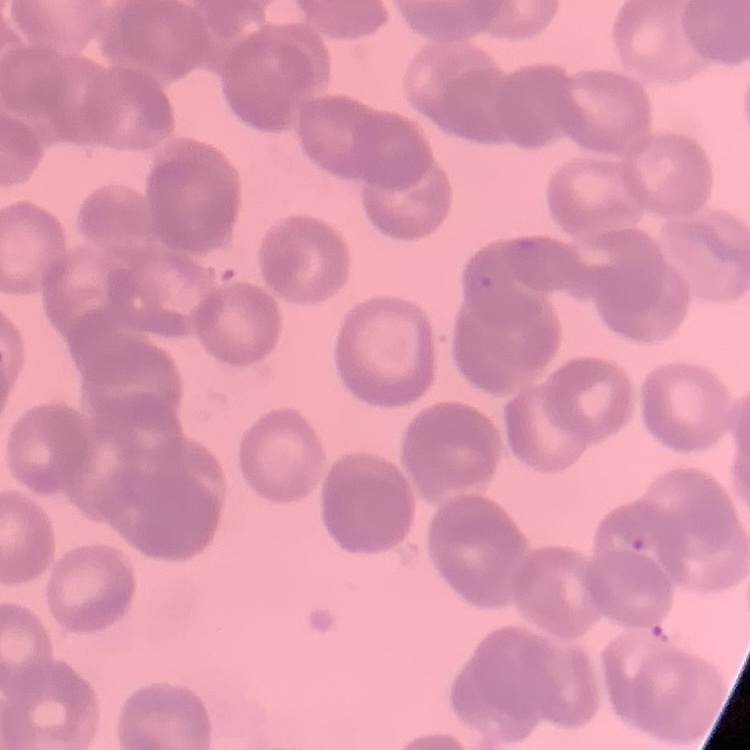
red blood cell morphology = rouleaux formation
stain = Field's or Giemsa
preparation = thin blood smear
image type = one tile cut from a larger photomicrograph